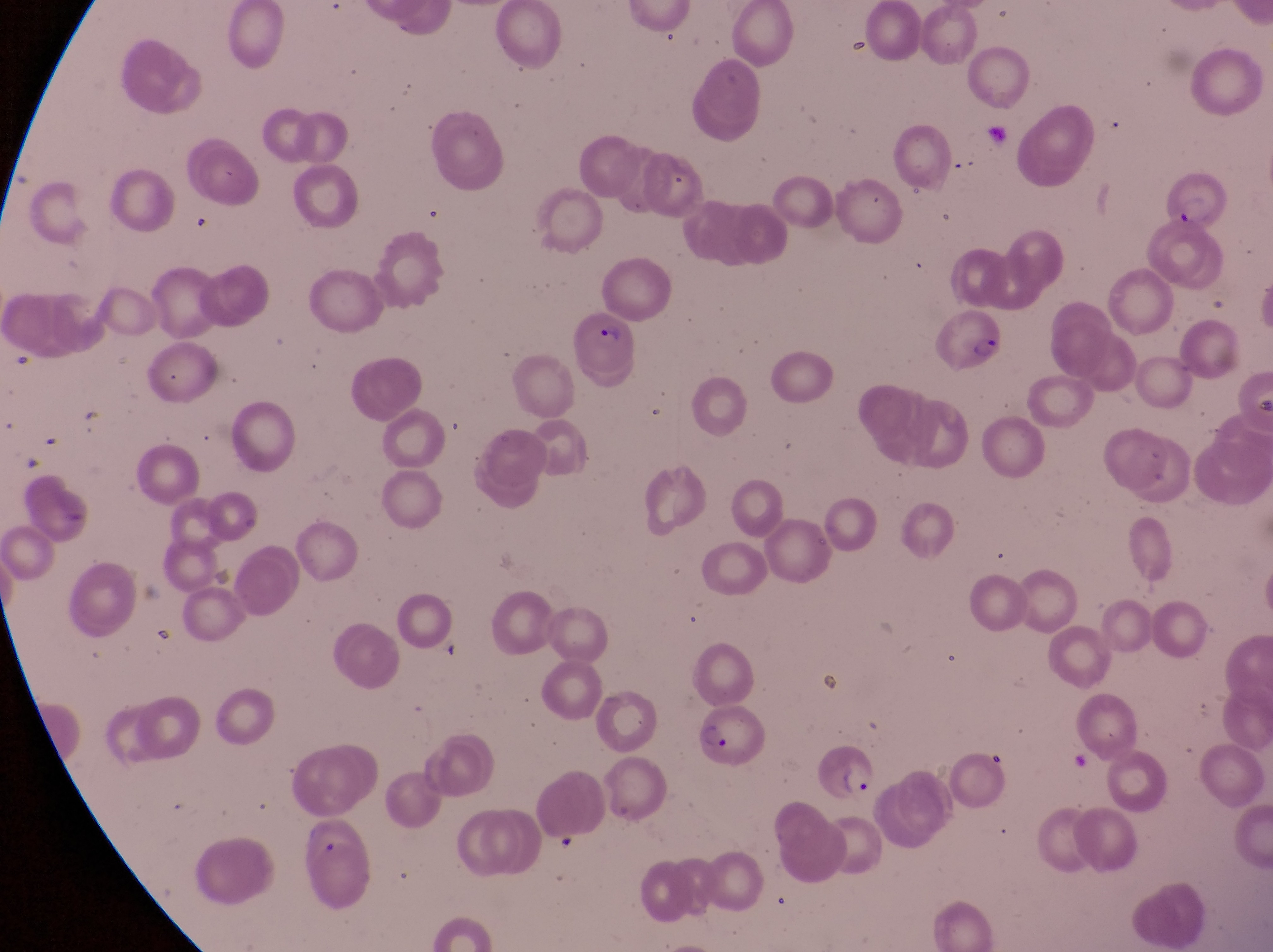

parasitised red blood cell locations = approximate bounding boxes as [left, top, right, bottom] in pixels: [1146, 164, 1223, 232], [936, 310, 1006, 377], [569, 312, 644, 374], [692, 704, 770, 769], [806, 741, 876, 808]
preparation = thin blood smear
magnification = 1000x
image size = 1273×952 pixels
capture = smartphone photograph through the eyepiece of an Olympus CX-23 microscope
country = Uganda
field of view = single